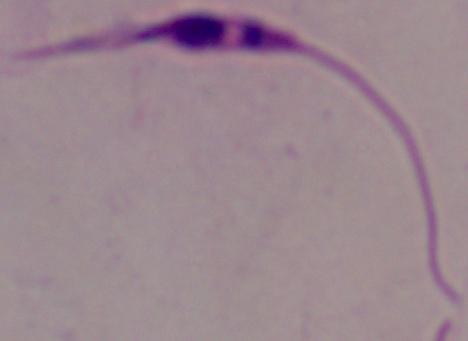

Summary:
  - Identification: Leishmania
  - Magnification: 1000x
  - Modality: micrograph